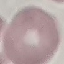 Result: no malaria parasites seen. Thin blood film. Giemsa stain. Cell patch, automatically extracted from a larger field of view and resized to 64 × 64 pixels. Photographed with a smartphone camera at the microscope eyepiece.